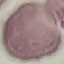

Summary:
  - Result: no malaria parasites detected
  - Stain: Giemsa
  - Image type: cell patch, automatically extracted from a larger field of view and resized to 64 × 64 pixels
  - Capture: smartphone through the microscope eyepiece
  - Preparation: thin blood film